Assess this cell for malaria.
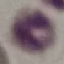
It is uninfected.

preparation = thin smear
capture = smartphone camera at the microscope eyepiece
image type = automatically extracted cell patch, resized to 64 × 64 pixels
stain = Giemsa